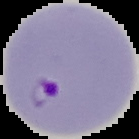

Summary:
  - Malaria status: parasitized
  - Preparation: thin blood film
  - Image type: segmented cell region with the area outside set to black
  - Image size: 139×139 pixels